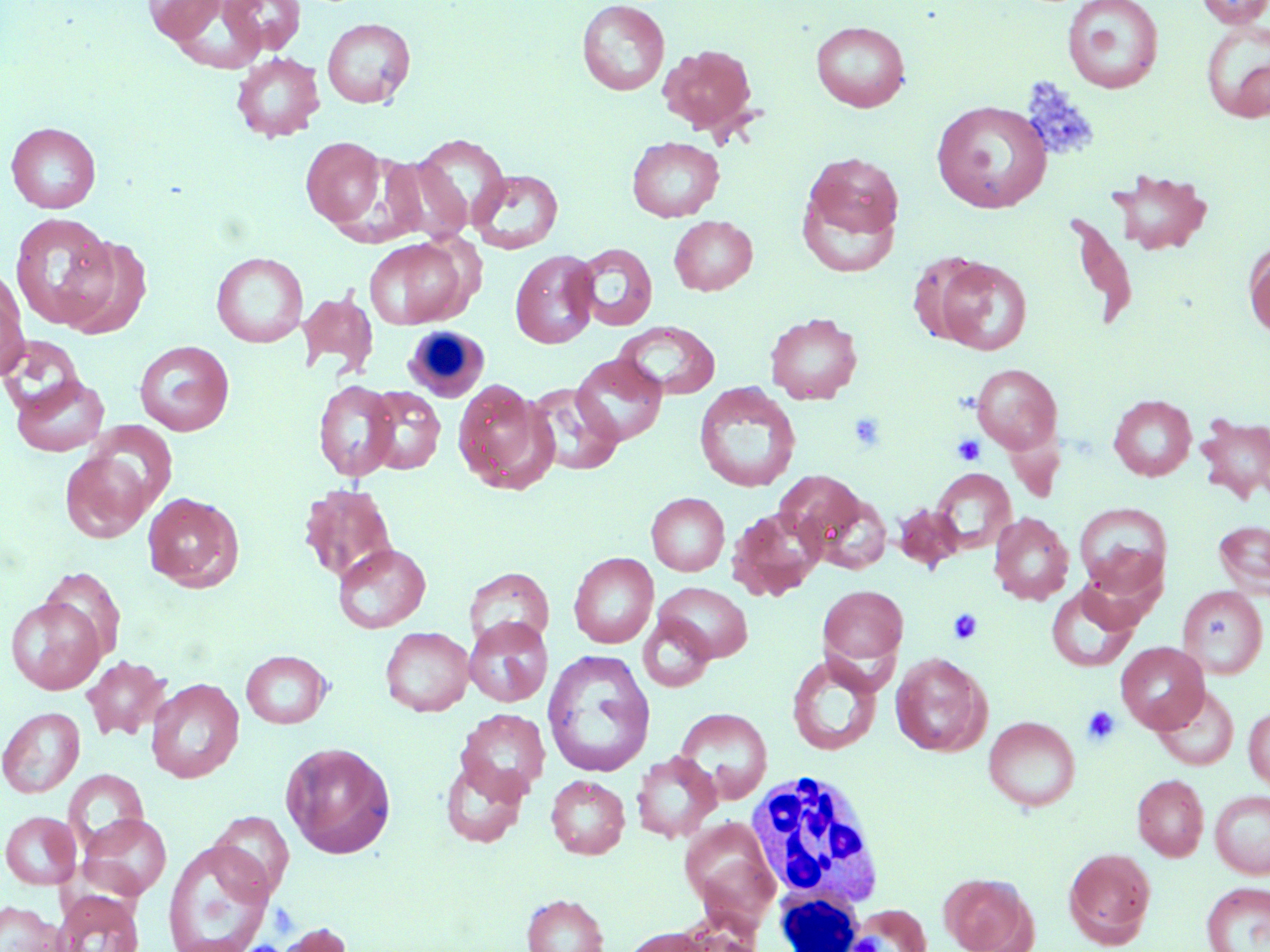

Approximate bounding boxes as (x1, y1, x2, y2) in pixels. White blood cell locations: (402, 325, 490, 402), (744, 769, 887, 914), (773, 892, 863, 951). Platelet locations: (1018, 78, 1100, 161), (848, 412, 888, 452), (951, 434, 986, 466), (948, 608, 984, 645), (1081, 706, 1120, 745), (849, 934, 884, 951). Uninfected red blood cell locations: (144, 0, 225, 43), (577, 0, 670, 95), (1061, 0, 1164, 94), (1195, 0, 1270, 29), (219, 1, 306, 56), (322, 17, 416, 108), (1200, 20, 1270, 122), (811, 21, 911, 112), (659, 43, 759, 137), (231, 52, 325, 142), (931, 100, 1052, 214), (6, 122, 101, 213), (410, 134, 511, 234), (301, 136, 386, 228), (627, 137, 724, 222), (800, 149, 905, 258), (378, 156, 471, 244), (469, 169, 563, 254), (1108, 170, 1213, 256), (1066, 210, 1139, 331), (10, 212, 115, 328), (670, 216, 758, 295), (57, 235, 152, 339), (364, 237, 473, 329), (572, 243, 658, 331), (1244, 243, 1270, 338), (510, 249, 600, 348), (211, 252, 308, 348), (907, 252, 992, 345), (934, 257, 1031, 355), (1, 270, 29, 378), (298, 288, 378, 380), (765, 312, 862, 404), (613, 321, 721, 401), (0, 335, 87, 421), (134, 340, 235, 436), (571, 354, 667, 446), (971, 364, 1062, 454), (10, 372, 110, 457), (313, 379, 400, 481), (453, 380, 558, 495), (693, 382, 801, 493), (525, 383, 623, 476), (364, 386, 446, 475), (1108, 394, 1197, 481), (1196, 413, 1270, 506), (87, 422, 178, 512), (60, 447, 154, 543), (930, 468, 1016, 555), (776, 471, 868, 555), (299, 484, 397, 585), (806, 488, 893, 575), (143, 492, 243, 591), (646, 492, 730, 576), (1074, 502, 1172, 597), (894, 503, 963, 572), (728, 506, 826, 601), (989, 513, 1074, 604), (1213, 519, 1270, 600), (333, 543, 430, 632), (569, 552, 659, 648), (1079, 557, 1163, 631), (39, 567, 126, 665), (464, 567, 554, 651), (655, 582, 753, 663), (818, 585, 908, 668), (1045, 585, 1139, 672), (1177, 585, 1268, 679), (6, 596, 106, 694), (638, 614, 715, 692), (464, 617, 553, 707), (380, 627, 473, 716), (1116, 642, 1209, 733), (542, 649, 655, 777), (241, 650, 331, 729), (891, 653, 990, 756), (81, 655, 171, 740), (786, 655, 882, 755), (146, 678, 244, 783), (1152, 685, 1239, 771), (0, 706, 84, 798), (1244, 706, 1270, 790), (675, 707, 773, 803), (456, 708, 551, 801), (983, 716, 1080, 812), (282, 742, 396, 858), (631, 751, 721, 843), (439, 756, 530, 848), (64, 769, 148, 851), (1132, 774, 1209, 861), (546, 775, 630, 859), (1210, 790, 1270, 878), (209, 810, 294, 898), (1, 811, 81, 889), (79, 813, 172, 899), (679, 817, 780, 928), (163, 839, 275, 952), (1063, 847, 1156, 947), (941, 873, 1036, 951), (1201, 882, 1270, 952), (52, 891, 144, 952), (521, 894, 609, 952), (0, 901, 66, 952), (847, 904, 930, 952), (668, 914, 767, 952), (269, 922, 354, 952), (619, 926, 717, 952). Slide-level diagnosis: negative for blood parasites. Image is 1270×952 pixels. Optical microscopy. 1000x magnification. Thin blood smear. Single field of view. May-Grünwald-Giemsa stain.